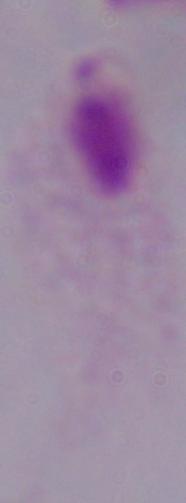
1000x magnification. Micrograph. A trichomonad is seen.